State the blood parasite species.
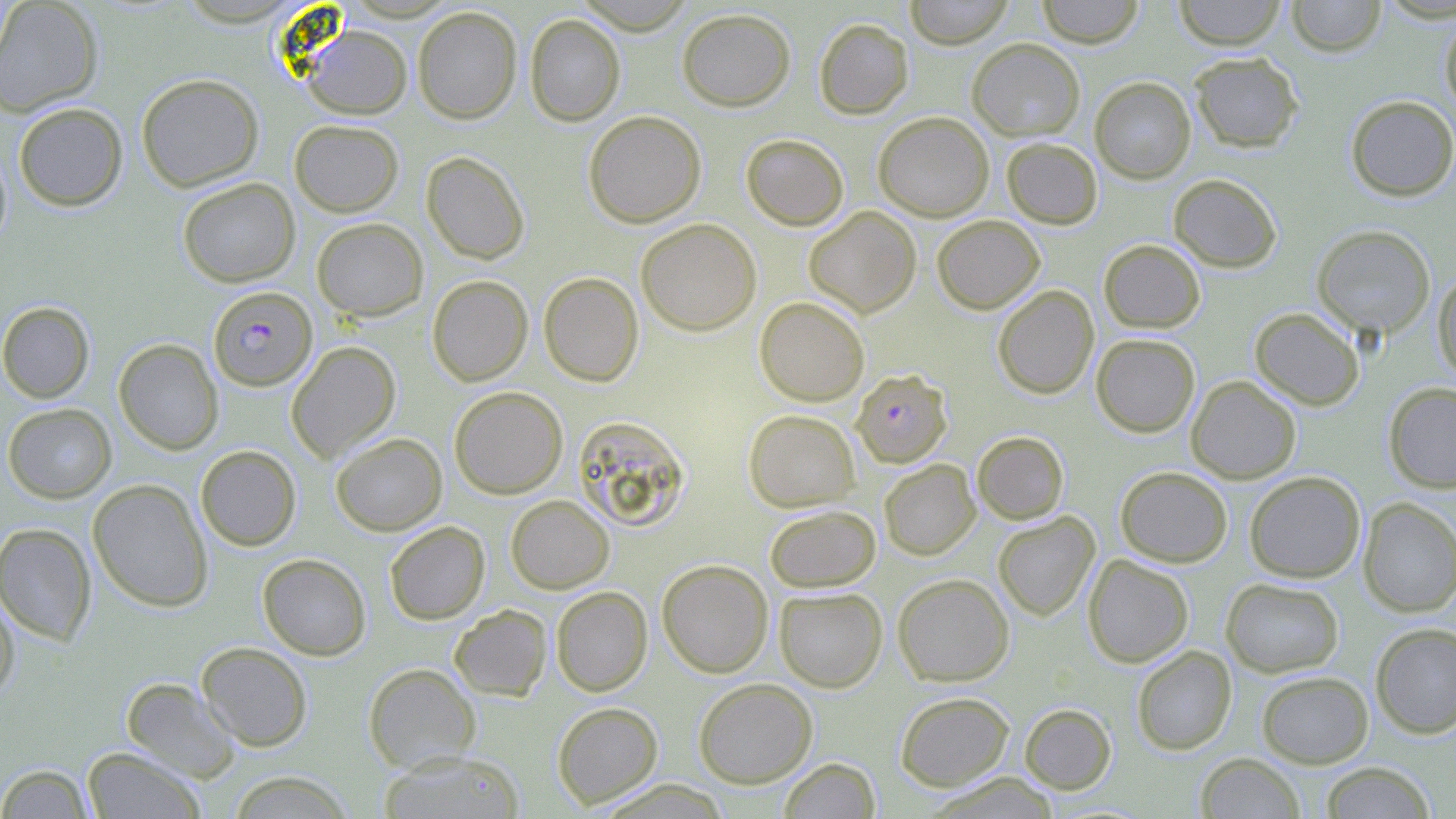
Plasmodium falciparum.

Approximate bounding boxes as [x1, y1, x2, y2] in pixels. Plasmodium falciparum-infected red blood cell locations: [208, 287, 317, 390], [852, 369, 952, 467]. Uninfected red blood cell locations: [0, 0, 104, 117], [904, 0, 1014, 48], [1036, 0, 1144, 47], [1173, 0, 1287, 50], [1286, 0, 1386, 56], [412, 6, 522, 124], [677, 7, 795, 111], [525, 13, 625, 126], [1440, 15, 1456, 115], [814, 17, 914, 119], [302, 24, 412, 119], [967, 38, 1085, 140], [1189, 52, 1304, 152], [136, 73, 264, 192], [1090, 76, 1195, 183], [1345, 95, 1456, 201], [13, 102, 128, 211], [583, 110, 706, 228], [873, 111, 994, 221], [289, 119, 404, 216], [741, 133, 849, 230], [1002, 137, 1102, 228], [0, 144, 12, 252], [421, 151, 529, 265], [1168, 173, 1282, 272], [177, 177, 300, 287], [804, 206, 921, 317], [932, 214, 1044, 314], [312, 217, 428, 321], [636, 218, 762, 336], [1312, 225, 1436, 339], [1099, 239, 1205, 333], [1433, 270, 1456, 380], [539, 272, 643, 387], [427, 275, 532, 386], [992, 285, 1099, 399], [754, 296, 869, 406], [0, 301, 95, 403], [1249, 307, 1364, 410], [1091, 334, 1200, 437], [114, 338, 223, 454], [286, 341, 400, 462], [1186, 375, 1301, 483], [1383, 382, 1456, 493], [449, 386, 568, 498], [3, 403, 117, 503], [743, 409, 859, 511], [573, 415, 691, 531], [972, 431, 1069, 524], [331, 432, 447, 535], [195, 445, 301, 550], [879, 459, 980, 560], [1115, 466, 1232, 567], [1244, 471, 1365, 583], [88, 479, 213, 612], [506, 495, 614, 594], [1358, 499, 1456, 617], [764, 504, 880, 592], [992, 511, 1100, 620], [384, 521, 490, 624], [0, 523, 96, 645], [257, 553, 371, 660], [1083, 554, 1194, 667], [657, 559, 773, 678], [892, 573, 1014, 686], [1221, 577, 1344, 677], [551, 587, 652, 696], [774, 587, 887, 692], [0, 591, 19, 701], [449, 604, 552, 701], [1371, 622, 1456, 738], [196, 642, 313, 751], [1132, 645, 1237, 755], [363, 662, 481, 773], [1257, 671, 1373, 768], [121, 677, 241, 782], [694, 678, 818, 788], [894, 691, 1014, 790], [552, 702, 663, 809], [1019, 703, 1116, 794], [82, 747, 205, 818], [378, 751, 526, 819], [1196, 753, 1305, 818], [779, 758, 880, 819], [1320, 761, 1436, 818], [0, 763, 95, 819], [224, 771, 356, 818], [926, 772, 1063, 819]. Thin blood smear. Optical microscopy. Image is 1456×819 pixels. May-Grünwald-Giemsa-stained preparation. Captured at 1000x magnification. Single field of view.